Identify the blood parasite species.
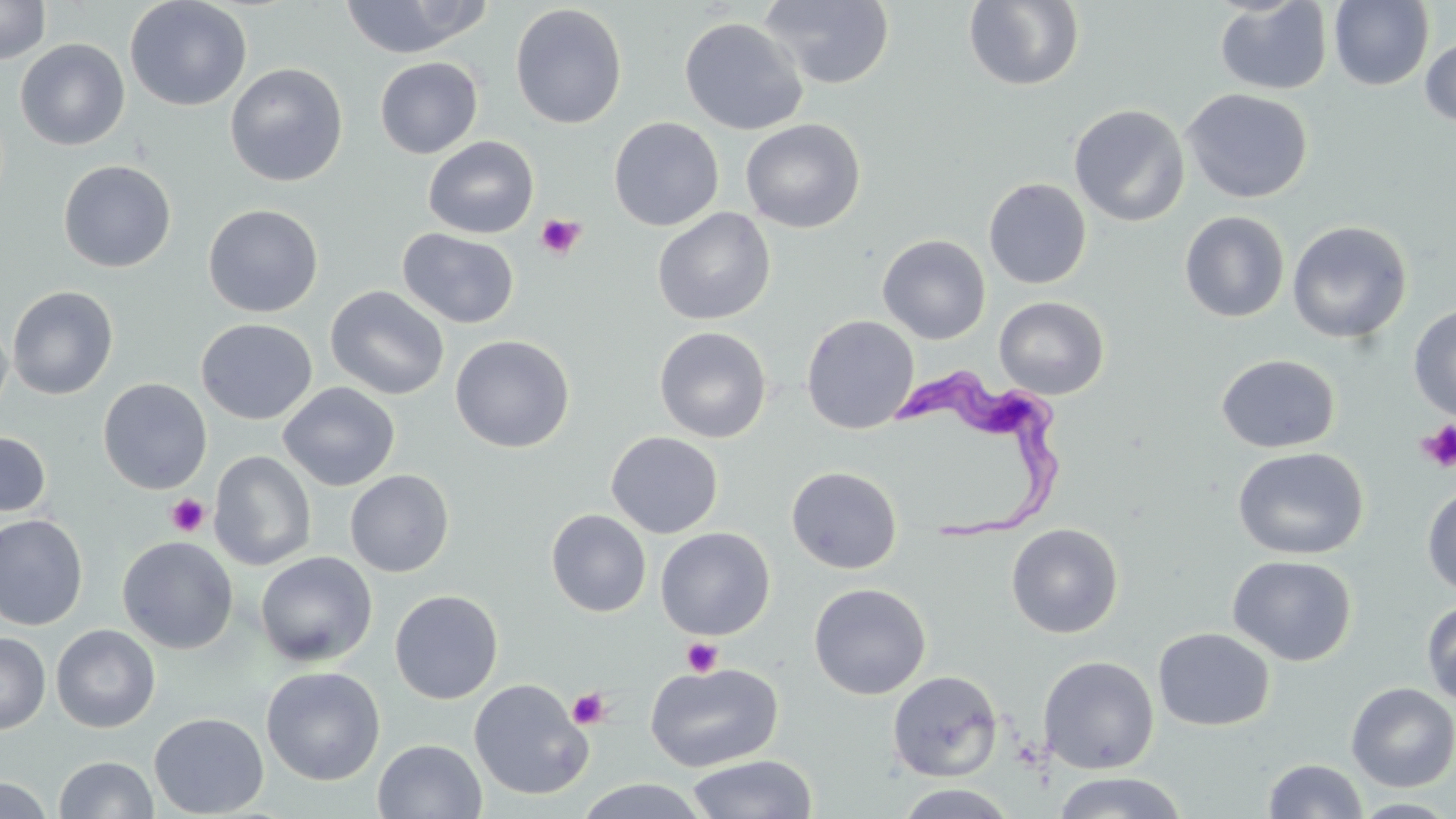
Trypanosoma brucei.

Approximate bounding boxes as (x1, y1, x2, y2) in pixels. Trypanosoma brucei locations: (893, 358, 1063, 538). Uninfected red blood cell locations: (124, 0, 252, 111), (338, 0, 491, 58), (1329, 0, 1433, 90), (0, 1, 51, 64), (758, 1, 894, 88), (963, 1, 1085, 91), (1214, 1, 1332, 95), (510, 4, 627, 129), (679, 17, 809, 135), (1419, 35, 1456, 127), (15, 38, 130, 151), (375, 56, 483, 158), (226, 62, 348, 187), (1181, 88, 1313, 204), (1068, 104, 1190, 227), (608, 116, 724, 231), (741, 118, 865, 233), (423, 136, 539, 239), (58, 159, 177, 272), (983, 178, 1091, 289), (202, 204, 323, 318), (652, 207, 775, 325), (1179, 211, 1290, 323), (1287, 221, 1412, 344), (398, 228, 519, 328), (877, 234, 991, 344), (6, 285, 119, 399), (325, 285, 450, 400), (994, 296, 1109, 400), (1408, 304, 1456, 422), (0, 312, 13, 425), (801, 314, 920, 434), (196, 318, 317, 425), (654, 326, 772, 443), (450, 334, 574, 452), (1215, 353, 1340, 454), (97, 378, 213, 494), (278, 382, 400, 491), (0, 431, 51, 517), (606, 431, 723, 538), (1232, 446, 1369, 560), (208, 450, 316, 571), (786, 465, 902, 575), (345, 470, 454, 577), (1421, 483, 1456, 597), (546, 509, 651, 617), (0, 514, 88, 631), (1006, 523, 1124, 638), (655, 527, 775, 640), (117, 535, 238, 654), (255, 551, 378, 667), (1227, 554, 1357, 666), (809, 583, 931, 699), (389, 589, 503, 704), (1421, 599, 1456, 706), (51, 624, 160, 733), (1153, 627, 1275, 731), (0, 632, 50, 734), (1038, 655, 1159, 774), (645, 661, 784, 772), (261, 665, 385, 785), (887, 670, 1003, 782), (468, 678, 593, 801), (1345, 681, 1456, 792), (149, 712, 269, 818), (373, 739, 487, 819), (686, 754, 818, 819), (54, 756, 158, 818), (1263, 759, 1368, 818), (1051, 771, 1189, 818), (1, 776, 53, 819), (572, 778, 712, 819), (895, 783, 1018, 818), (1349, 798, 1456, 818). Platelet locations: (535, 213, 585, 259), (1417, 422, 1456, 472), (166, 493, 210, 537), (681, 637, 723, 677), (567, 687, 611, 730). May-Grünwald-Giemsa stain. 1000x magnification. Optical microscopy. Thin blood film. Image is 1456×819 pixels. One field of a larger specimen.